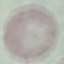
Result: no malaria parasites detected. Thin blood smear. Acquired by smartphone through the microscope eyepiece. Giemsa stain. Cell patch, automatically extracted from a larger field of view and resized to 64 × 64 pixels.